Assess this cell for malaria.
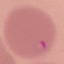
Parasitized.

Acquired by smartphone through the microscope eyepiece. Thin smear of blood. Automatically extracted cell patch, resized to 64 × 64 pixels. Giemsa stain.